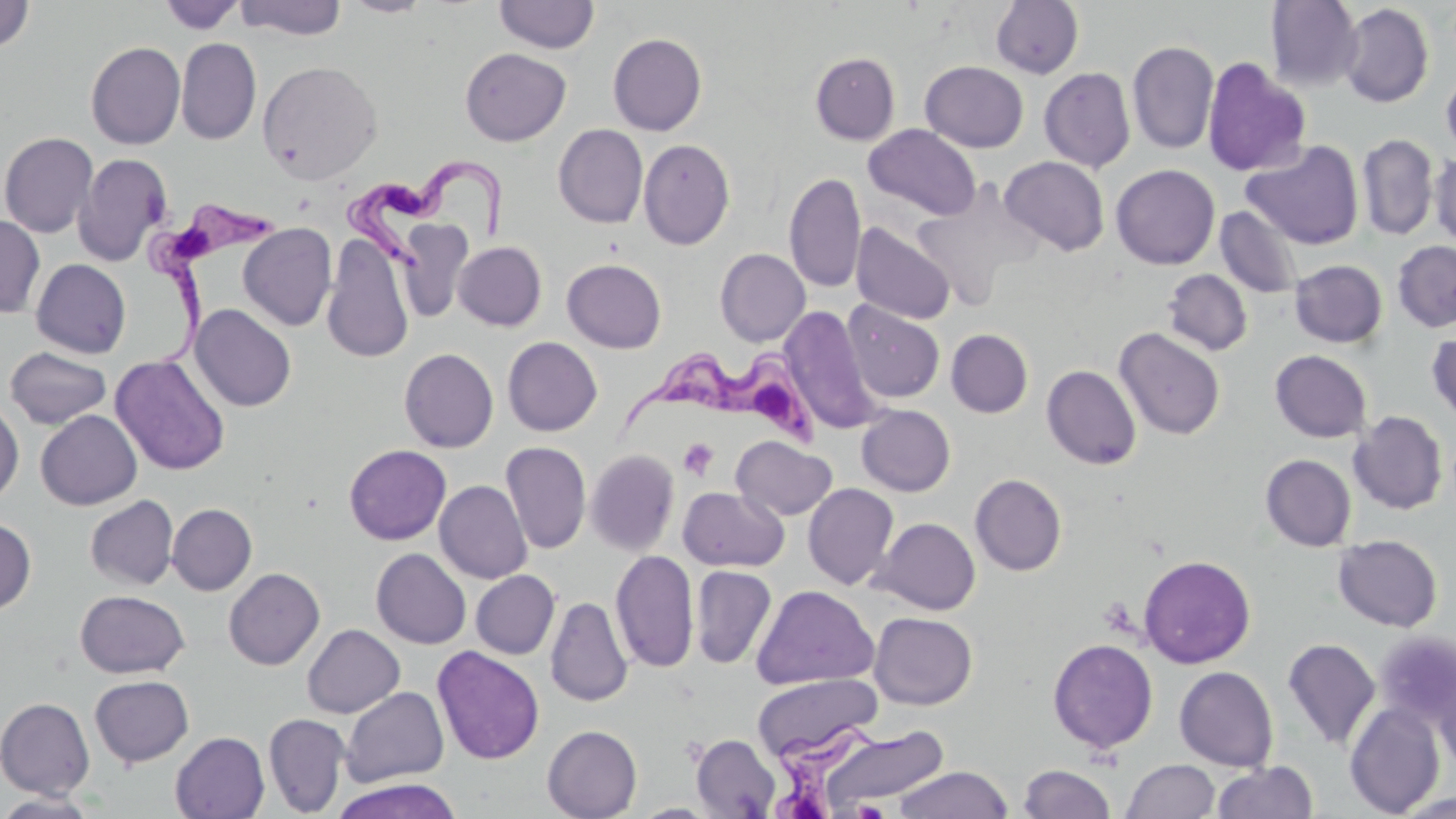

{
  "slide_level_diagnosis": "Trypanosoma brucei",
  "platelet_locations": "approximate bounding boxes as [x1, y1, x2, y2] in pixels: [678, 437, 718, 480]",
  "preparation": "thin blood film",
  "field_of_view": "single",
  "trypanosoma_brucei_locations": "approximate bounding boxes as [x1, y1, x2, y2] in pixels: [338, 159, 515, 269], [141, 200, 286, 364], [617, 334, 824, 451], [760, 719, 926, 819]",
  "magnification": "1000x",
  "uninfected_red_blood_cell_locations": "approximate bounding boxes as [x1, y1, x2, y2] in pixels: [158, 0, 245, 34], [235, 0, 347, 40], [342, 0, 433, 17], [990, 0, 1084, 78], [1, 1, 34, 53], [494, 1, 600, 54], [1265, 1, 1363, 91], [1339, 3, 1433, 108], [607, 33, 707, 135], [176, 38, 261, 145], [1127, 41, 1219, 154], [85, 42, 186, 150], [460, 47, 571, 146], [810, 52, 900, 144], [1201, 56, 1312, 177], [257, 60, 383, 184], [921, 61, 1029, 152], [1039, 67, 1136, 172], [1440, 68, 1456, 162], [553, 124, 648, 228], [864, 124, 981, 220], [0, 131, 98, 238], [1358, 134, 1438, 241], [638, 139, 735, 250], [1242, 140, 1365, 250], [1430, 152, 1456, 248], [73, 153, 172, 267], [1000, 156, 1110, 255], [1111, 164, 1220, 269], [784, 172, 867, 293], [1216, 206, 1302, 299], [395, 214, 477, 324], [0, 215, 45, 318], [851, 222, 956, 325], [238, 223, 337, 331], [322, 235, 414, 364], [453, 241, 546, 331], [1392, 241, 1456, 332], [715, 248, 810, 347], [562, 258, 666, 353], [31, 259, 131, 359], [1289, 260, 1387, 348], [1162, 269, 1253, 355], [843, 301, 945, 404], [190, 305, 297, 413], [781, 306, 882, 434], [1115, 327, 1225, 440], [946, 329, 1033, 418], [1427, 329, 1456, 425], [502, 337, 602, 436], [5, 347, 112, 429], [399, 348, 498, 453], [1270, 350, 1372, 443], [110, 354, 231, 476], [1042, 365, 1142, 471], [0, 398, 24, 505], [856, 405, 956, 496], [36, 410, 142, 510], [1349, 411, 1448, 514], [731, 435, 837, 521], [501, 442, 591, 554], [344, 444, 451, 545], [585, 449, 680, 556], [1260, 454, 1356, 551], [970, 473, 1067, 576], [434, 480, 532, 584], [803, 483, 899, 590], [678, 486, 788, 571], [85, 495, 179, 589], [167, 504, 256, 595], [0, 517, 36, 613], [873, 517, 981, 614], [1333, 534, 1443, 632], [371, 548, 471, 649], [610, 550, 699, 673], [1138, 555, 1256, 668], [690, 565, 777, 669], [224, 568, 325, 670], [471, 570, 560, 659], [751, 585, 878, 689], [74, 590, 189, 678], [545, 597, 632, 707], [869, 612, 977, 710], [302, 624, 404, 718], [1373, 630, 1456, 727], [1047, 638, 1158, 754], [1282, 638, 1380, 751], [432, 645, 544, 765], [1174, 666, 1279, 771], [1433, 671, 1456, 777], [752, 674, 881, 761], [89, 675, 194, 767], [340, 687, 449, 787], [0, 697, 95, 799], [1344, 701, 1445, 816], [263, 713, 349, 817], [542, 725, 642, 819], [820, 725, 950, 812], [170, 732, 269, 819], [691, 733, 781, 819], [1121, 760, 1220, 818], [1212, 760, 1318, 819], [1018, 764, 1117, 819], [895, 766, 1013, 819], [328, 778, 465, 819], [0, 791, 99, 817], [1393, 791, 1456, 818], [630, 803, 721, 818]",
  "modality": "light microscopy",
  "stain": "May-Grünwald-Giemsa",
  "image_size": "1456×819 pixels"
}